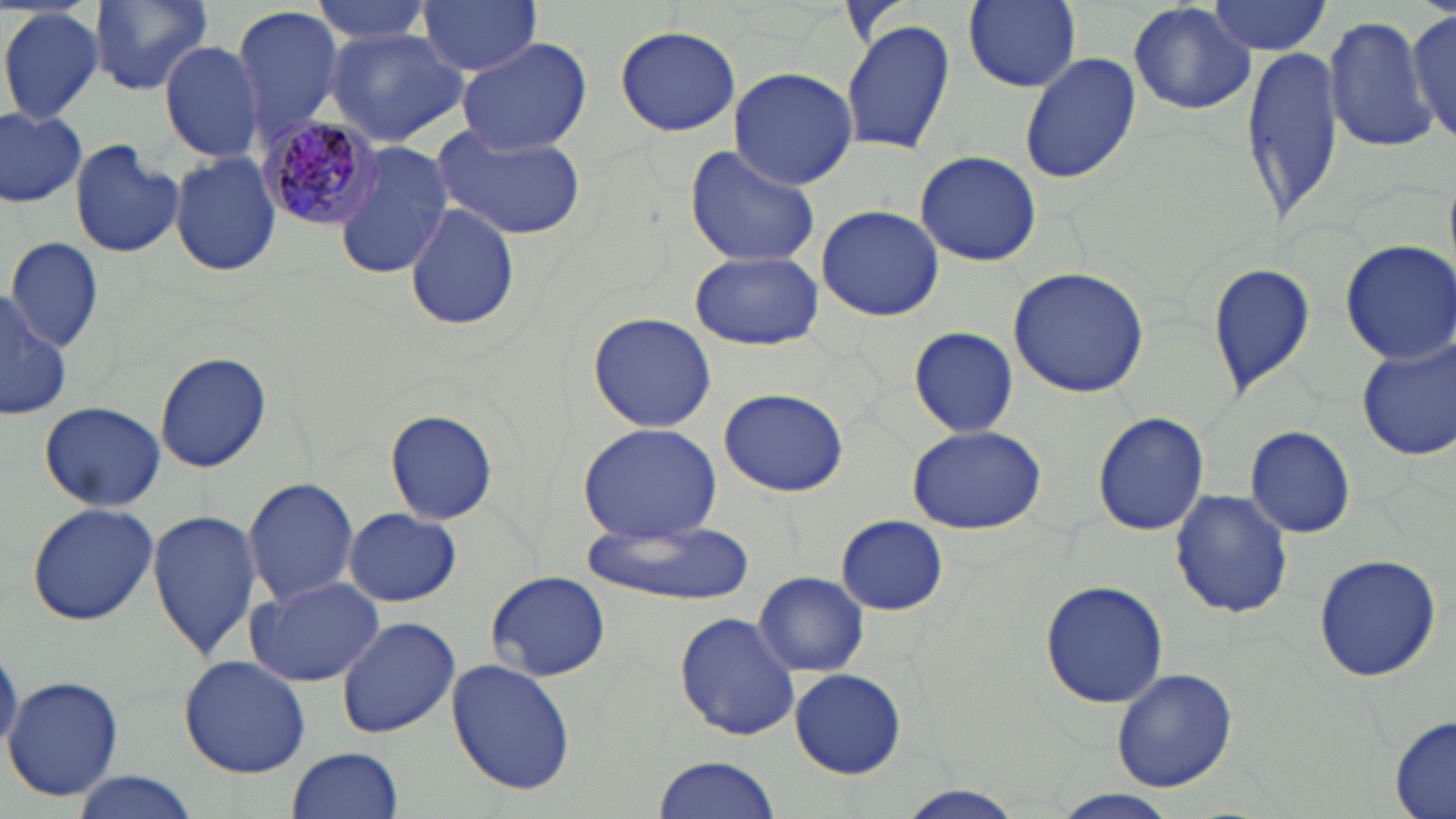
slide_level_diagnosis: Plasmodium malariae
magnification: 1000x
preparation: thin blood film
modality: optical microscopy
uninfected_red_blood_cell_locations: 'approximate bounding boxes as named x1/y1/x2/y2 corners in pixels: (x1=89, y1=0, x2=213, y2=94), (x1=314, y1=0, x2=439, y2=45), (x1=417, y1=0, x2=542, y2=75), (x1=959, y1=0, x2=1085, y2=95), (x1=1127, y1=0, x2=1257, y2=116), (x1=1205, y1=0, x2=1335, y2=56), (x1=0, y1=6, x2=103, y2=125), (x1=231, y1=6, x2=343, y2=144), (x1=1406, y1=7, x2=1456, y2=146), (x1=1323, y1=16, x2=1439, y2=152), (x1=841, y1=19, x2=956, y2=157), (x1=615, y1=26, x2=741, y2=136), (x1=324, y1=27, x2=470, y2=148), (x1=456, y1=36, x2=591, y2=154), (x1=160, y1=39, x2=264, y2=166), (x1=1243, y1=41, x2=1346, y2=229), (x1=1020, y1=52, x2=1140, y2=184), (x1=729, y1=66, x2=857, y2=189), (x1=0, y1=107, x2=87, y2=206), (x1=432, y1=125, x2=587, y2=240), (x1=69, y1=138, x2=185, y2=259), (x1=332, y1=139, x2=451, y2=280), (x1=684, y1=145, x2=820, y2=269), (x1=915, y1=149, x2=1041, y2=267), (x1=168, y1=151, x2=282, y2=278), (x1=405, y1=200, x2=520, y2=334), (x1=815, y1=207, x2=944, y2=321), (x1=5, y1=235, x2=104, y2=351), (x1=1340, y1=240, x2=1456, y2=364), (x1=685, y1=251, x2=826, y2=349), (x1=1205, y1=260, x2=1317, y2=399), (x1=1007, y1=267, x2=1151, y2=397), (x1=0, y1=287, x2=73, y2=422), (x1=585, y1=312, x2=717, y2=432), (x1=909, y1=328, x2=1017, y2=437), (x1=1356, y1=335, x2=1456, y2=461), (x1=154, y1=350, x2=272, y2=473), (x1=719, y1=388, x2=848, y2=495), (x1=38, y1=401, x2=165, y2=511), (x1=384, y1=408, x2=499, y2=527), (x1=1091, y1=411, x2=1210, y2=537), (x1=574, y1=422, x2=723, y2=542), (x1=907, y1=422, x2=1047, y2=533), (x1=1245, y1=425, x2=1357, y2=539), (x1=243, y1=477, x2=361, y2=608), (x1=1169, y1=488, x2=1294, y2=617), (x1=26, y1=502, x2=158, y2=625), (x1=148, y1=510, x2=263, y2=660), (x1=343, y1=510, x2=463, y2=606), (x1=836, y1=516, x2=948, y2=615), (x1=580, y1=520, x2=750, y2=608), (x1=1312, y1=554, x2=1441, y2=683), (x1=485, y1=571, x2=610, y2=681), (x1=755, y1=573, x2=869, y2=675), (x1=244, y1=576, x2=387, y2=685), (x1=1037, y1=578, x2=1169, y2=708), (x1=674, y1=610, x2=801, y2=741), (x1=335, y1=614, x2=461, y2=739), (x1=0, y1=640, x2=22, y2=756), (x1=178, y1=653, x2=314, y2=777), (x1=446, y1=660, x2=576, y2=795), (x1=789, y1=668, x2=907, y2=779), (x1=1111, y1=668, x2=1238, y2=791), (x1=5, y1=675, x2=124, y2=804), (x1=1391, y1=713, x2=1456, y2=819), (x1=287, y1=747, x2=402, y2=819), (x1=650, y1=754, x2=785, y2=819), (x1=69, y1=773, x2=204, y2=819), (x1=893, y1=786, x2=1029, y2=817), (x1=1057, y1=790, x2=1179, y2=817)'
field_of_view: single
stain: May-Grünwald-Giemsa
plasmodium_malariae_infected_red_blood_cell_locations: 'approximate bounding boxes as named x1/y1/x2/y2 corners in pixels: (x1=258, y1=115, x2=381, y2=230)'
image_size: 1456×819 pixels